Assess this cell for malaria.
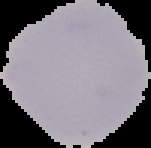

Uninfected.

Summary:
  - Image type: cell region segmented out of the field of view; surrounding area masked to black
  - Preparation: thin blood smear
  - Image size: 151×148 pixels